Assess this cell for malaria.
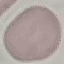
Uninfected.

Summary:
  - Preparation: thin blood smear
  - Stain: Giemsa
  - Image type: cell patch, automatically extracted from a larger field of view and resized to 64 × 64 pixels
  - Capture: smartphone camera at the microscope eyepiece